Comment on the morphology of the red blood cells.
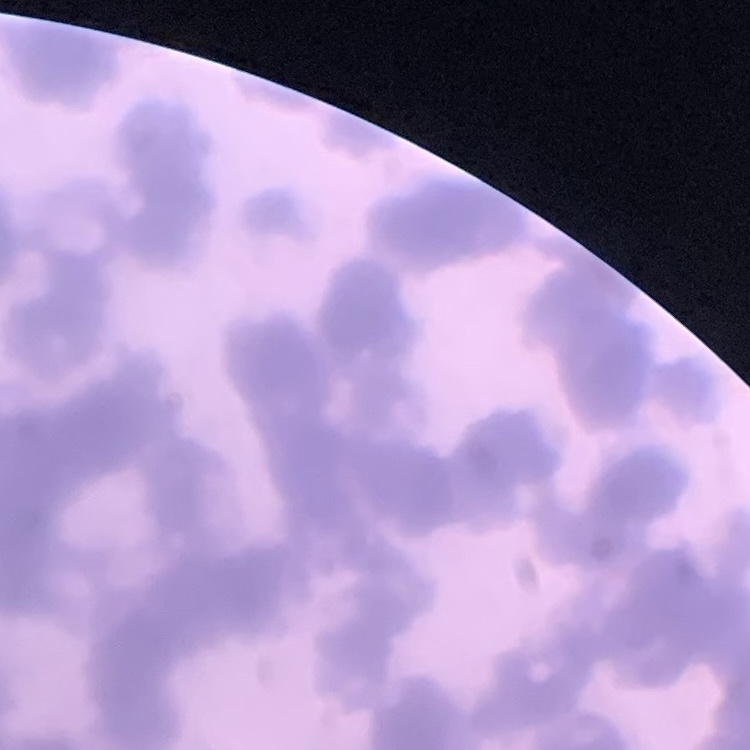

Rouleaux formation.

stain = Field's or Giemsa
preparation = thin peripheral smear
image type = square crop of a larger photomicrograph